Comment on the morphology of the erythrocytes.
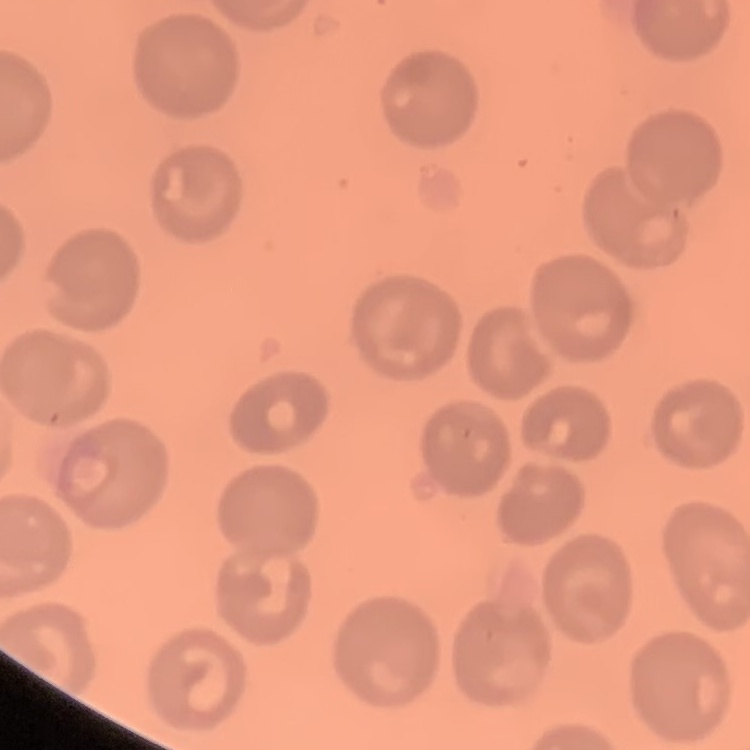

They show no rouleaux formation.

image type = one tile cut from a larger photomicrograph
stain = Field's or Giemsa
preparation = thin blood smear